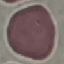
result = no malaria parasites detected
preparation = thin blood film
stain = Giemsa
capture = smartphone camera at the microscope eyepiece
image type = cell patch, automatically extracted from a larger field of view and resized to 64 × 64 pixels